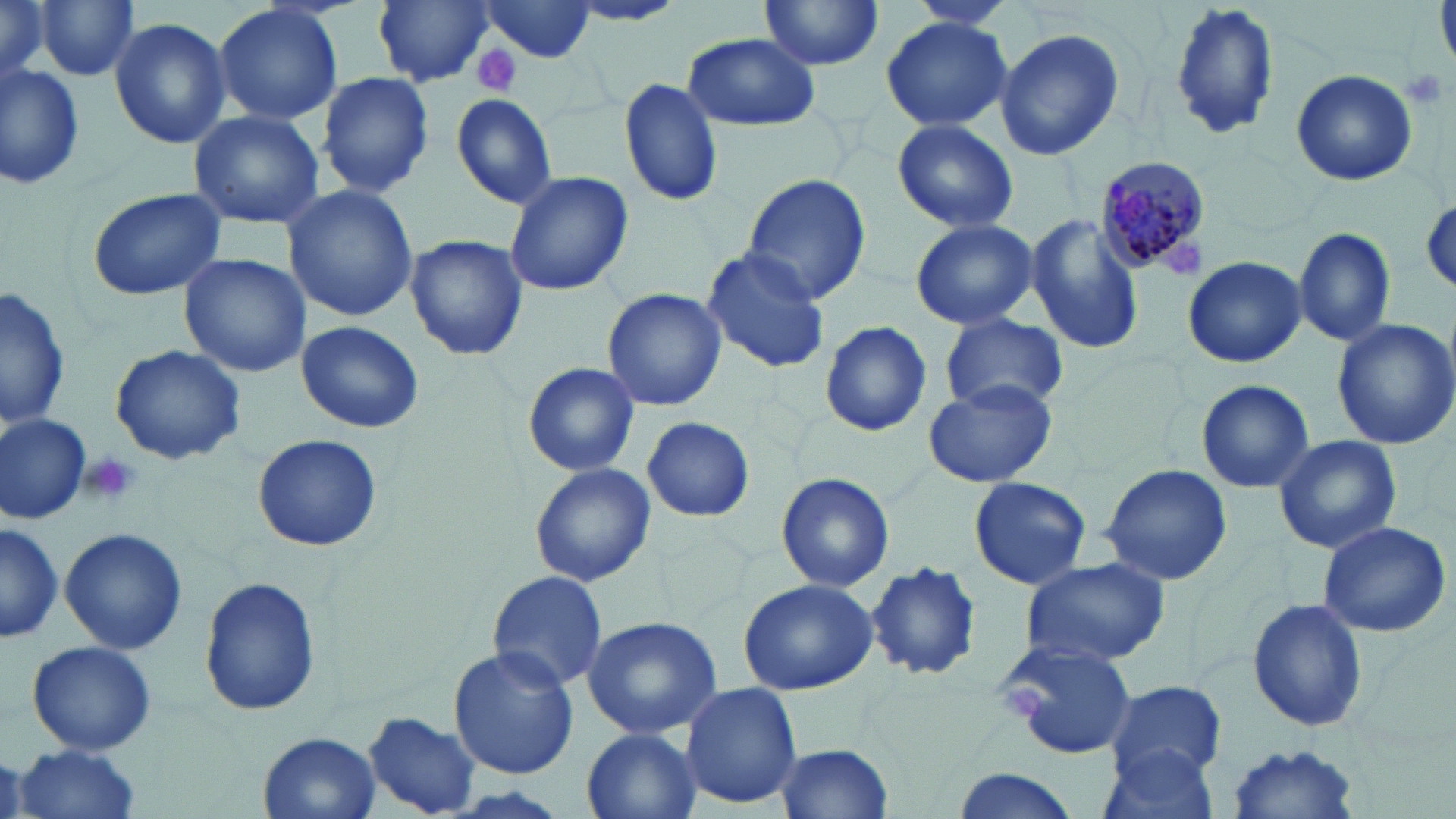

Summary:
  - Coordinate format: approximate bounding boxes as [x1, y1, x2, y2] in pixels
  - Uninfected red blood cell locations: [0, 0, 53, 83], [37, 0, 140, 83], [372, 0, 493, 87], [758, 0, 884, 72], [906, 0, 1018, 33], [1167, 0, 1279, 144], [213, 1, 343, 128], [479, 3, 599, 63], [565, 3, 686, 28], [879, 16, 1014, 133], [111, 18, 231, 149], [993, 24, 1125, 161], [680, 34, 821, 133], [1, 60, 85, 189], [1290, 68, 1419, 187], [316, 70, 436, 198], [619, 77, 724, 208], [450, 93, 557, 209], [190, 109, 326, 229], [890, 119, 1018, 235], [503, 171, 634, 298], [740, 173, 873, 303], [281, 183, 418, 323], [86, 188, 225, 300], [1023, 214, 1142, 356], [910, 218, 1039, 331], [1295, 227, 1395, 350], [403, 234, 528, 360], [700, 246, 831, 375], [179, 252, 310, 377], [1182, 255, 1305, 368], [2, 284, 71, 431], [603, 288, 729, 413], [941, 312, 1067, 413], [297, 319, 424, 433], [1333, 319, 1456, 447], [818, 322, 934, 438], [110, 345, 245, 465], [521, 360, 641, 478], [922, 377, 1057, 489], [1196, 379, 1314, 495], [0, 413, 91, 523], [642, 416, 754, 523], [253, 433, 382, 552], [1273, 434, 1402, 554], [530, 462, 657, 587], [1100, 463, 1233, 586], [776, 471, 896, 592], [967, 476, 1091, 590], [1318, 521, 1452, 638], [1, 523, 64, 642], [59, 528, 187, 654], [1019, 556, 1170, 668], [865, 564, 983, 681], [486, 571, 610, 695], [738, 575, 879, 696], [200, 576, 322, 716], [1245, 599, 1371, 732], [580, 616, 724, 741], [998, 636, 1139, 758], [27, 641, 157, 755], [448, 646, 579, 778], [1104, 680, 1229, 781], [679, 681, 803, 809], [363, 711, 481, 815], [581, 727, 703, 818], [259, 731, 380, 818], [774, 740, 895, 819], [1097, 743, 1223, 819], [15, 744, 143, 819], [1222, 745, 1364, 819], [948, 766, 1085, 819]
  - Platelet locations: [471, 47, 520, 96], [1399, 67, 1449, 112], [1165, 244, 1206, 279], [82, 449, 141, 505], [1007, 685, 1047, 717]
  - Plasmodium malariae-infected red blood cell locations: [1093, 154, 1216, 279]
  - Slide-level diagnosis: Plasmodium malariae
  - Preparation: thin blood smear
  - Stain: May-Grünwald-Giemsa
  - Magnification: 1000x
  - Modality: light microscopy
  - Field of view: single
  - Image size: 1456×819 pixels